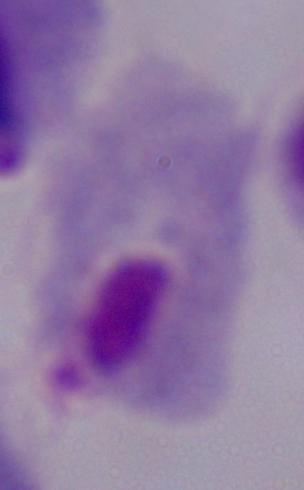
identification: trichomonad
modality: micrograph
magnification: 1000x